Identify the parasite.
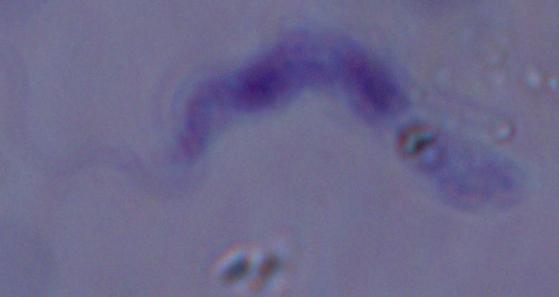

This is a trypanosome.

Summary:
  - Magnification: 1000x
  - Modality: photomicrograph